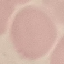

Summary:
  - Malaria status: uninfected
  - Image type: automatically extracted cell patch, resized to 64 × 64 pixels
  - Capture: smartphone through the microscope eyepiece
  - Stain: Giemsa
  - Preparation: thin blood film